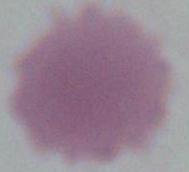
Captured at 1000x magnification. A red blood cell is shown. Micrograph.